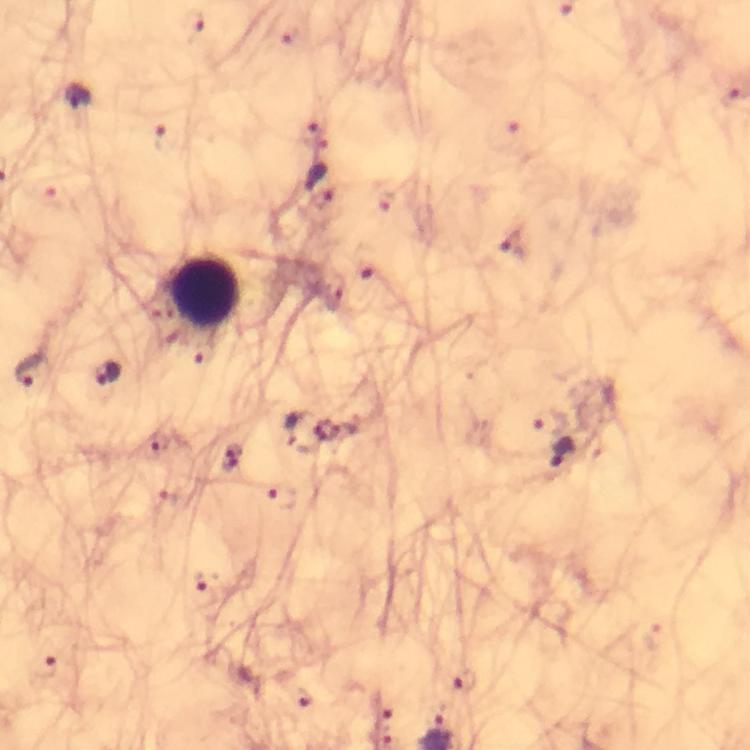

Approximate centers as [x, y] in pixels.
Summary:
  - Leukocyte locations: [205, 291]
  - Malaria parasite locations: [193, 23], [293, 35], [78, 98], [315, 133], [158, 137], [314, 176], [514, 242], [367, 262], [333, 291], [29, 370], [109, 373], [550, 422], [293, 428], [155, 443], [563, 452], [230, 457], [279, 496], [169, 504], [206, 596], [45, 667], [466, 681], [301, 699]
  - Magnification: 100x
  - Capture: smartphone camera through the microscope
  - Context: from a diagnostic examination for malaria
  - Preparation: thick blood film
  - Immersion oil: used
  - Stain: Giemsa
  - Cropped from: one field of view
  - Image size: 750×750 pixels